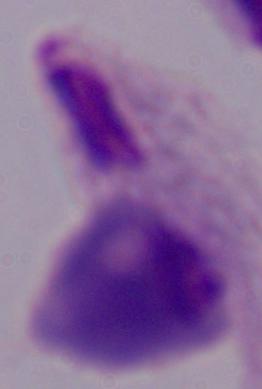
Summary:
  - Magnification: 1000x
  - Identification: trichomonad
  - Modality: photomicrograph